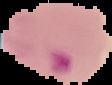 Cell region segmented out of the field of view; the surrounding area is masked to black. Image is 112×85 pixels. From a thin blood smear. Result: Plasmodium parasites detected.